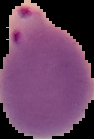

Image is 94×139 pixels. From a thin blood film. Segmented cell region on a black background. Malaria status: parasitized.